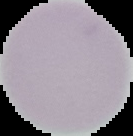 Segmented cell region on a black background. Malaria status: uninfected. Image is 133×136 pixels. From a thin blood film.